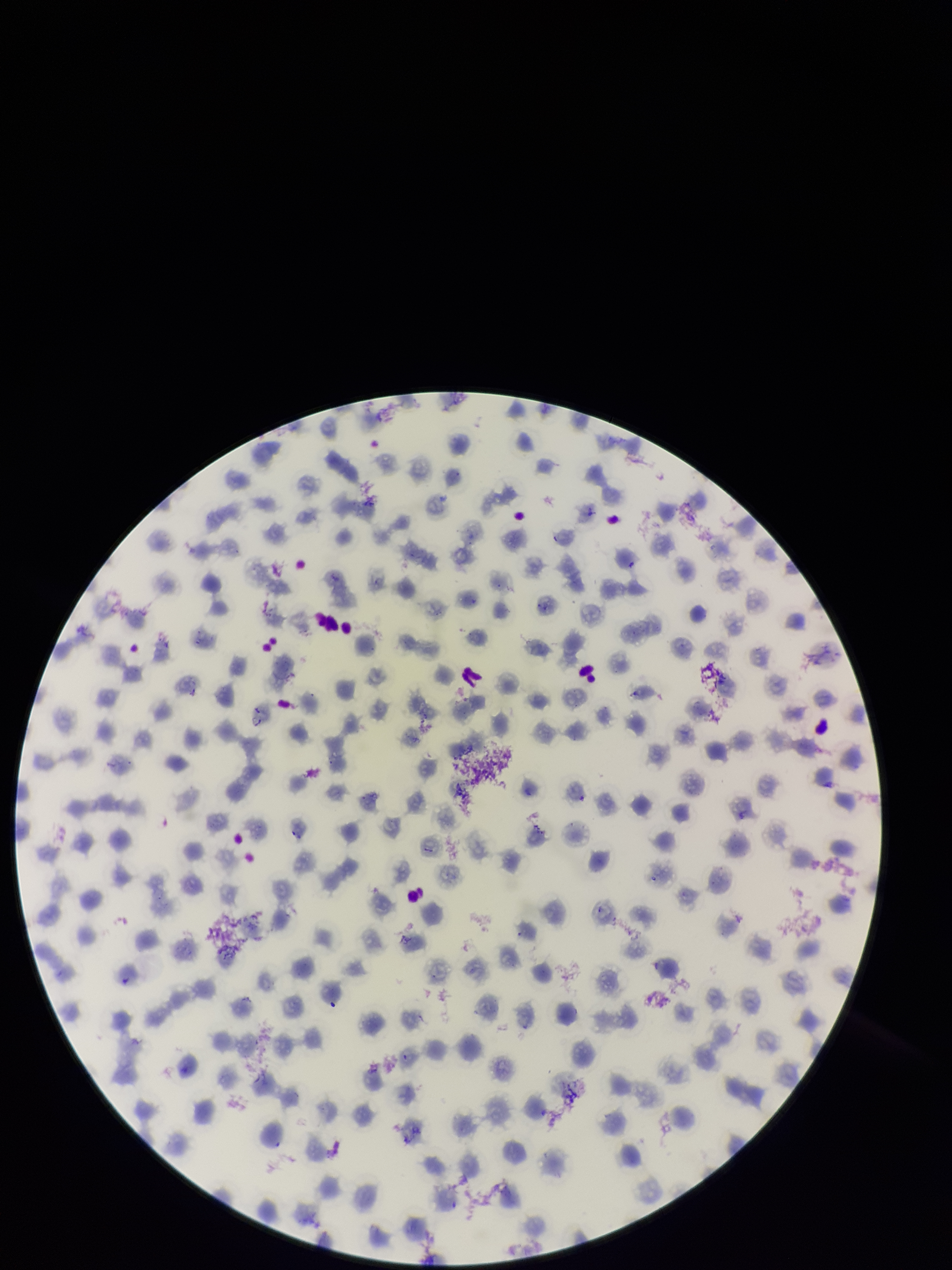
{
  "stain": "Giemsa",
  "patient_malaria_status": "positive",
  "capture": "smartphone photograph through the microscope eyepiece",
  "field_of_view": "one from this slide",
  "image_size": "952×1270 pixels",
  "parasitized_red_blood_cells": "none seen",
  "species_reported_for_this_patient": "Plasmodium falciparum",
  "preparation": "thin smear",
  "red_blood_cell_count": 160,
  "parasitized_red_blood_cell_count": 0
}